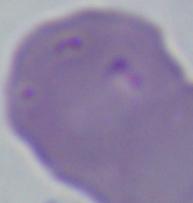

Captured at 1000x magnification. Photomicrograph. A Babesia parasite is seen.